State which parasite is depicted.
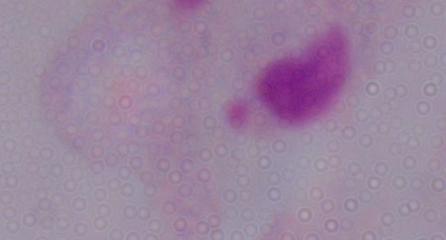

This is a trichomonad.

Summary:
  - Modality: photomicrograph
  - Magnification: 1000x